Report the malaria status of this cell.
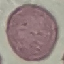

Uninfected.

Summary:
  - Image type: cell patch, automatically extracted from a larger field of view and resized to 64 × 64 pixels
  - Capture: smartphone camera at the microscope eyepiece
  - Preparation: thin smear
  - Stain: Giemsa